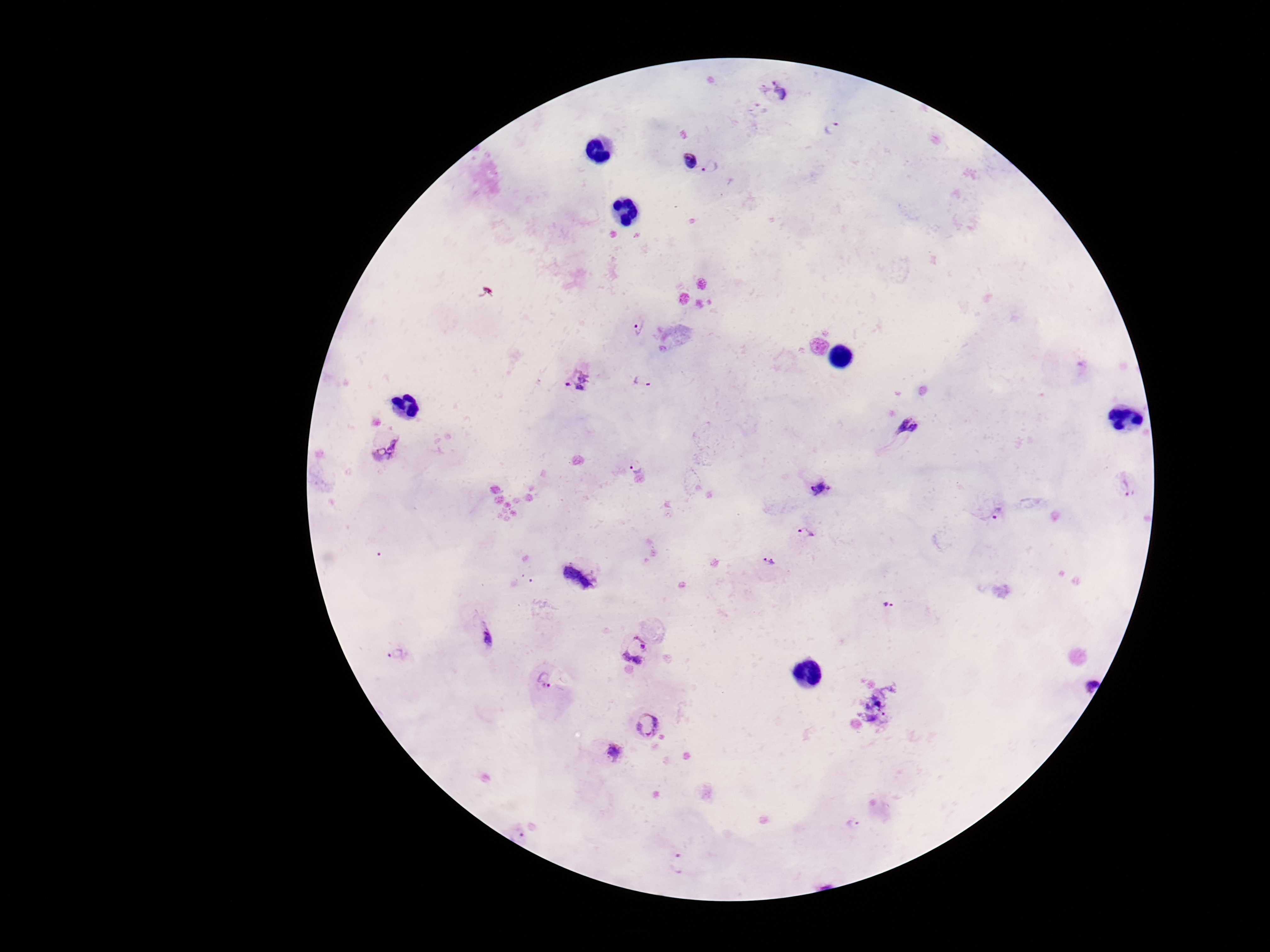
Approximate centers as [x, y] in pixels.
Summary:
  - Plasmodium parasite locations: [775, 91], [833, 128], [686, 160], [713, 168], [638, 326], [579, 378], [643, 380], [908, 429], [383, 445], [636, 465], [1128, 486], [820, 488], [996, 513], [803, 533], [769, 561], [582, 580], [887, 604], [487, 632], [640, 649], [397, 654], [547, 681], [1088, 682], [875, 709], [649, 725], [612, 752], [854, 823], [519, 834], [680, 861]
  - Field of view: one from this slide
  - Stain: Giemsa
  - Capture: smartphone camera through the microscope eyepiece
  - Preparation: thick blood film
  - Magnification: 100x
  - Image size: 1270×952 pixels
  - Patient malaria status: infected